Assess this cell for malaria.
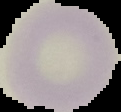

Uninfected.

Summary:
  - Preparation: thin blood film
  - Image type: segmented cell region on a black background
  - Image size: 121×112 pixels